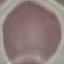 Malaria status: uninfected. Thin blood film. Acquired by smartphone through the microscope eyepiece. Cell patch, automatically extracted from a larger field of view and resized to 64 × 64 pixels. Giemsa stain.